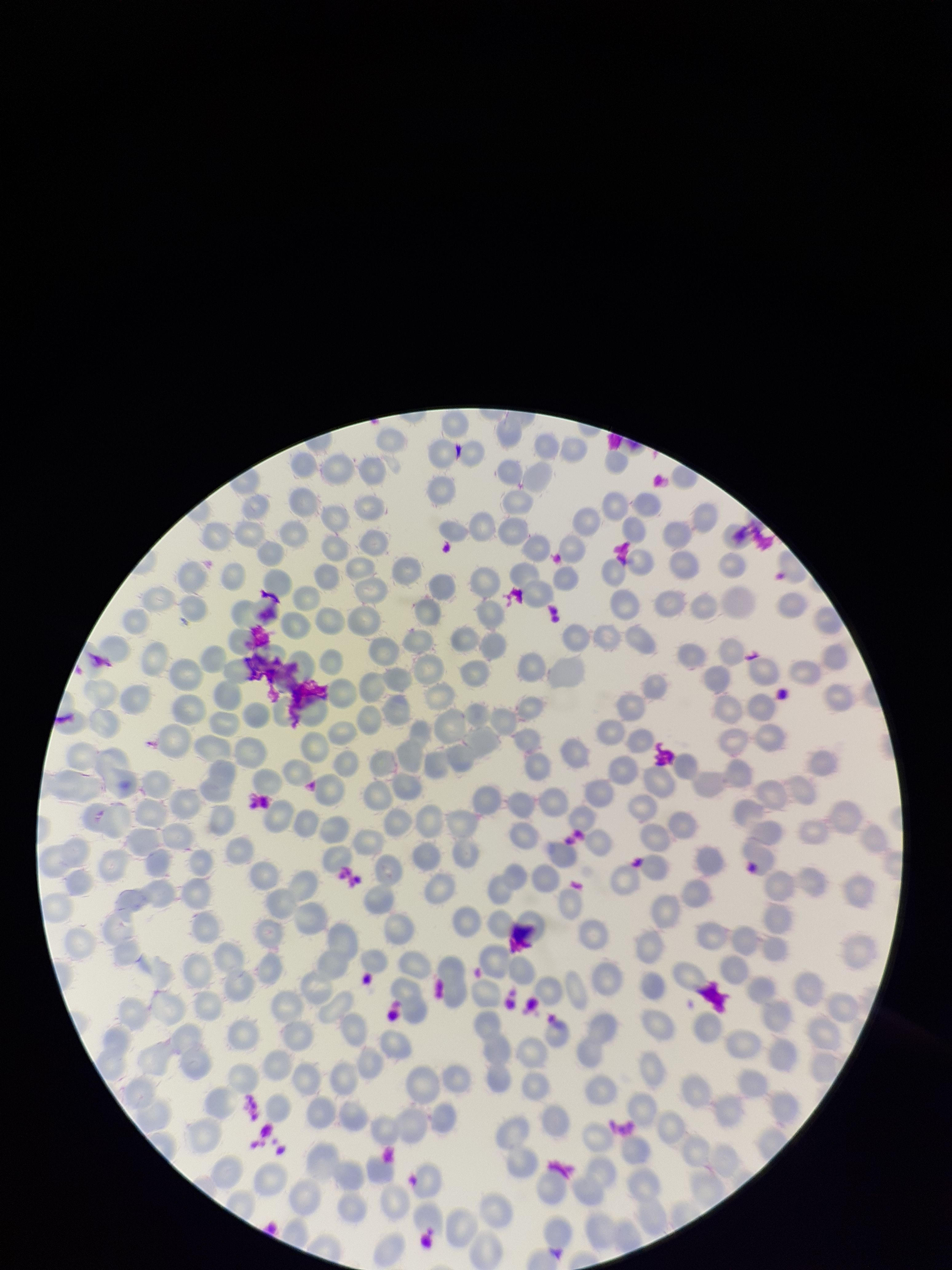

capture: smartphone photograph through the microscope eyepiece
red_blood_cell_count: 252
image_size: 952×1270 pixels
parasitized_red_blood_cells: none detected
parasitized_red_blood_cell_count: 0
stain: Giemsa
field_of_view: one from this slide
preparation: thin
patient_malaria_status: negative